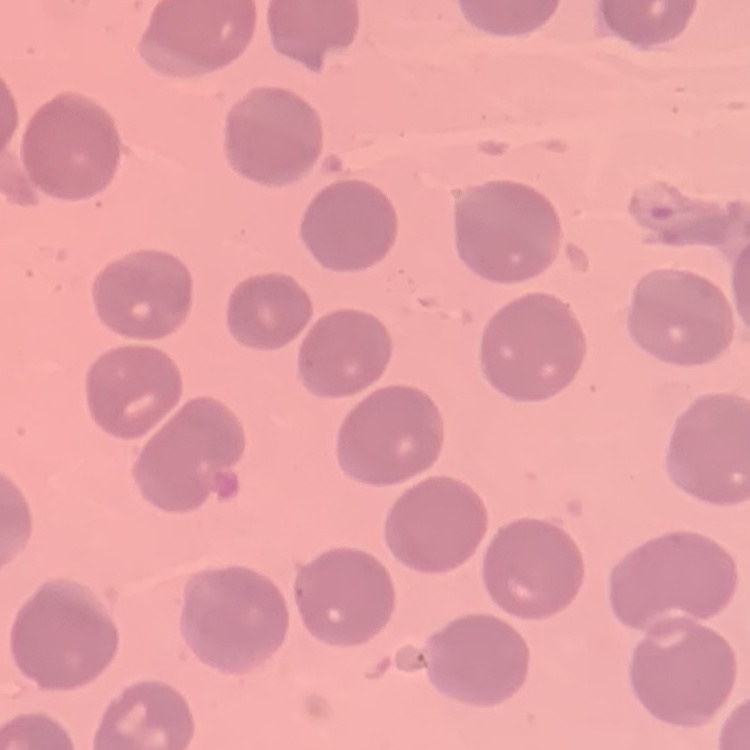
The erythrocytes show no rouleaux formation. Thin blood film. One tile cut from a larger photomicrograph. Stained with either Field's or Giemsa.